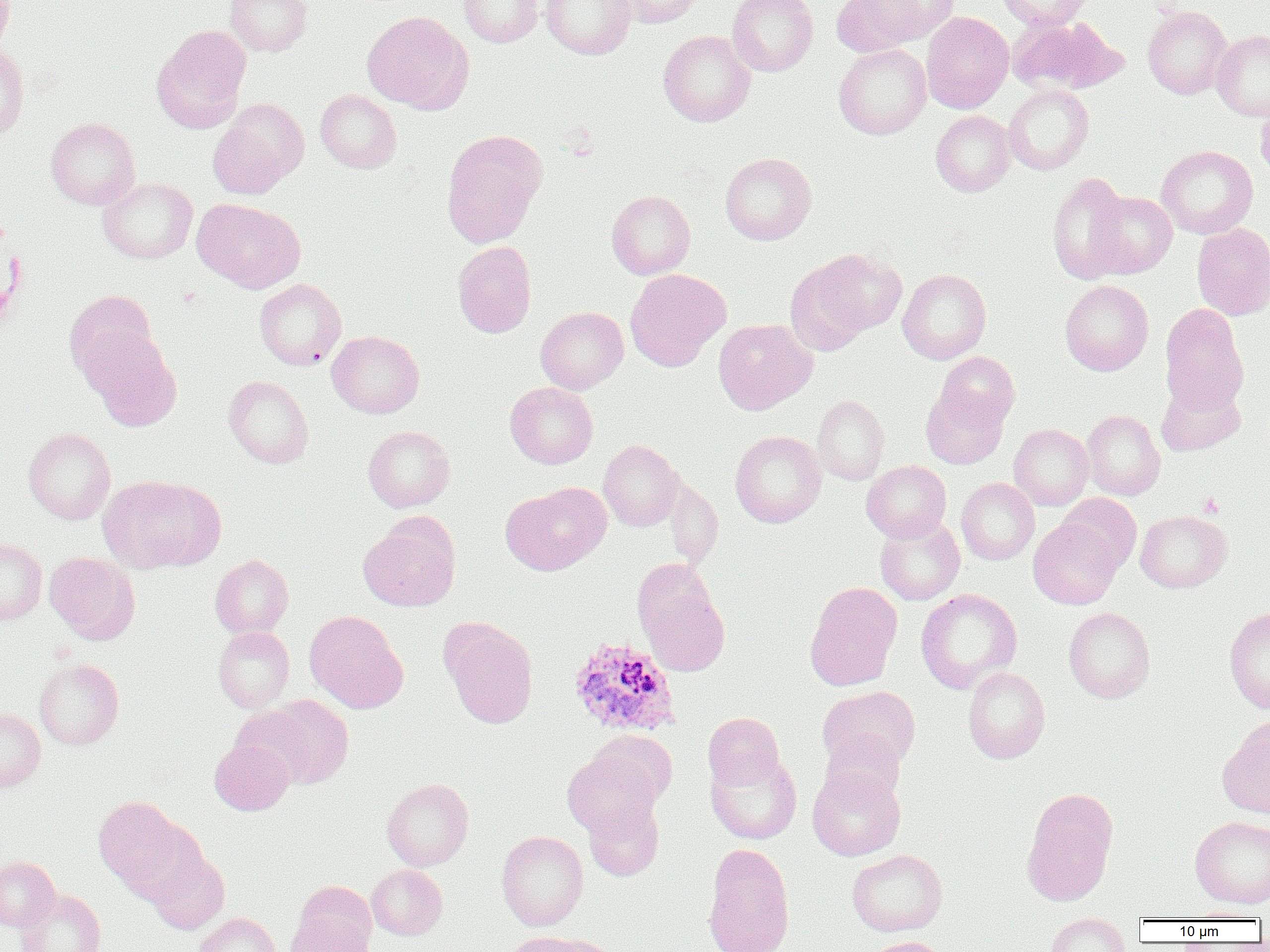

slide-level diagnosis = Plasmodium ovale
field of view = single
platelet locations = approximate bounding boxes as named x1/y1/x2/y2 corners in pixels: (x1=1199, y1=492, x2=1224, y2=518)
Plasmodium ovale-infected red blood cell locations = approximate bounding boxes as named x1/y1/x2/y2 corners in pixels: (x1=568, y1=638, x2=680, y2=736)
image size = 1270×952 pixels
magnification = 1000x
modality = light microscopy
preparation = thin blood smear
uninfected red blood cell locations = approximate bounding boxes as named x1/y1/x2/y2 corners in pixels: (x1=0, y1=0, x2=15, y2=57), (x1=225, y1=0, x2=312, y2=56), (x1=457, y1=0, x2=543, y2=47), (x1=540, y1=0, x2=637, y2=60), (x1=614, y1=0, x2=705, y2=27), (x1=727, y1=0, x2=819, y2=76), (x1=831, y1=0, x2=934, y2=57), (x1=865, y1=0, x2=960, y2=45), (x1=997, y1=0, x2=1092, y2=30), (x1=1143, y1=5, x2=1231, y2=99), (x1=362, y1=10, x2=474, y2=114), (x1=921, y1=11, x2=1014, y2=113), (x1=1006, y1=16, x2=1126, y2=95), (x1=151, y1=25, x2=252, y2=133), (x1=658, y1=30, x2=756, y2=126), (x1=1211, y1=30, x2=1270, y2=121), (x1=0, y1=44, x2=30, y2=139), (x1=834, y1=44, x2=932, y2=139), (x1=1004, y1=84, x2=1094, y2=175), (x1=315, y1=90, x2=401, y2=173), (x1=208, y1=98, x2=309, y2=197), (x1=1256, y1=98, x2=1270, y2=181), (x1=930, y1=110, x2=1015, y2=197), (x1=45, y1=118, x2=140, y2=209), (x1=441, y1=130, x2=546, y2=247), (x1=1156, y1=145, x2=1258, y2=239), (x1=720, y1=153, x2=817, y2=245), (x1=1047, y1=172, x2=1134, y2=284), (x1=99, y1=177, x2=197, y2=263), (x1=606, y1=190, x2=695, y2=279), (x1=1086, y1=190, x2=1177, y2=279), (x1=192, y1=198, x2=306, y2=293), (x1=1191, y1=223, x2=1270, y2=319), (x1=452, y1=241, x2=537, y2=338), (x1=787, y1=249, x2=902, y2=351), (x1=625, y1=268, x2=729, y2=371), (x1=898, y1=269, x2=991, y2=364), (x1=254, y1=278, x2=346, y2=370), (x1=1060, y1=280, x2=1153, y2=376), (x1=65, y1=290, x2=158, y2=382), (x1=1159, y1=304, x2=1249, y2=414), (x1=535, y1=306, x2=629, y2=394), (x1=713, y1=318, x2=817, y2=414), (x1=82, y1=330, x2=181, y2=430), (x1=327, y1=331, x2=424, y2=418), (x1=936, y1=352, x2=1020, y2=429), (x1=224, y1=375, x2=314, y2=468), (x1=1156, y1=380, x2=1245, y2=456), (x1=505, y1=382, x2=598, y2=469), (x1=921, y1=386, x2=1008, y2=469), (x1=812, y1=395, x2=889, y2=485), (x1=1081, y1=410, x2=1166, y2=500), (x1=1009, y1=424, x2=1093, y2=510), (x1=363, y1=425, x2=455, y2=512), (x1=23, y1=428, x2=115, y2=524), (x1=729, y1=430, x2=826, y2=528), (x1=598, y1=440, x2=685, y2=531), (x1=862, y1=460, x2=951, y2=543), (x1=98, y1=475, x2=225, y2=573), (x1=956, y1=478, x2=1039, y2=565), (x1=502, y1=483, x2=610, y2=576), (x1=1055, y1=493, x2=1141, y2=574), (x1=1135, y1=510, x2=1232, y2=592), (x1=358, y1=514, x2=461, y2=612), (x1=874, y1=515, x2=964, y2=605), (x1=1028, y1=519, x2=1122, y2=609), (x1=0, y1=538, x2=46, y2=625), (x1=45, y1=553, x2=140, y2=644), (x1=210, y1=555, x2=293, y2=638), (x1=632, y1=557, x2=718, y2=645), (x1=804, y1=582, x2=902, y2=691), (x1=641, y1=586, x2=730, y2=676), (x1=915, y1=589, x2=1022, y2=694), (x1=1064, y1=607, x2=1156, y2=703), (x1=1224, y1=607, x2=1270, y2=713), (x1=304, y1=610, x2=408, y2=713), (x1=440, y1=617, x2=538, y2=728), (x1=213, y1=626, x2=294, y2=713), (x1=34, y1=658, x2=124, y2=749), (x1=963, y1=667, x2=1050, y2=764), (x1=818, y1=685, x2=920, y2=773), (x1=256, y1=695, x2=354, y2=788), (x1=0, y1=706, x2=45, y2=792), (x1=702, y1=713, x2=784, y2=789), (x1=1218, y1=716, x2=1270, y2=819), (x1=589, y1=731, x2=678, y2=806), (x1=821, y1=731, x2=906, y2=804), (x1=209, y1=738, x2=295, y2=815), (x1=563, y1=750, x2=662, y2=837), (x1=705, y1=752, x2=802, y2=844), (x1=706, y1=760, x2=903, y2=848), (x1=807, y1=767, x2=905, y2=860), (x1=381, y1=778, x2=474, y2=871), (x1=1021, y1=794, x2=1116, y2=905), (x1=93, y1=795, x2=190, y2=894), (x1=583, y1=797, x2=664, y2=881), (x1=1190, y1=816, x2=1270, y2=908), (x1=497, y1=830, x2=588, y2=931), (x1=702, y1=843, x2=796, y2=952), (x1=846, y1=849, x2=948, y2=936), (x1=147, y1=850, x2=230, y2=935), (x1=0, y1=856, x2=59, y2=930), (x1=367, y1=865, x2=447, y2=940), (x1=295, y1=881, x2=377, y2=951), (x1=15, y1=888, x2=105, y2=952), (x1=1183, y1=908, x2=1267, y2=921), (x1=195, y1=913, x2=280, y2=952), (x1=1045, y1=913, x2=1131, y2=952), (x1=287, y1=916, x2=373, y2=952), (x1=503, y1=931, x2=597, y2=952), (x1=865, y1=936, x2=949, y2=952)